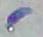
{
  "identification": "Toxoplasma gondii",
  "magnification": "1000x",
  "modality": "photomicrograph"
}